Assess this cell for malaria.
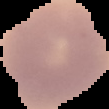

Uninfected.

image size = 109×109 pixels
preparation = thin blood film
image type = segmented cell region with the area outside set to black